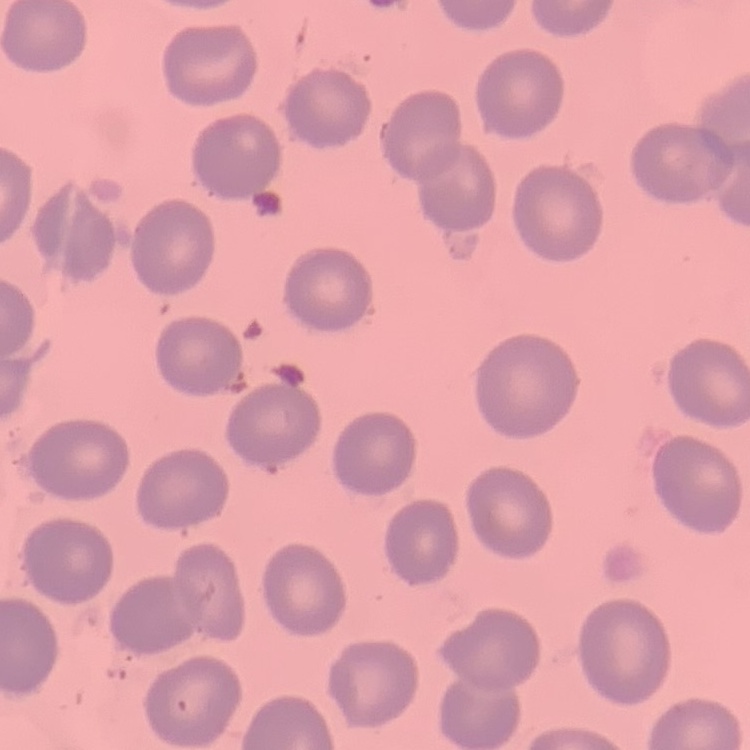 The red blood cells exhibit no rouleaux formation. Stained with either Field's or Giemsa. Thin peripheral smear. Square crop of a larger photomicrograph.